Identify the blood parasite species.
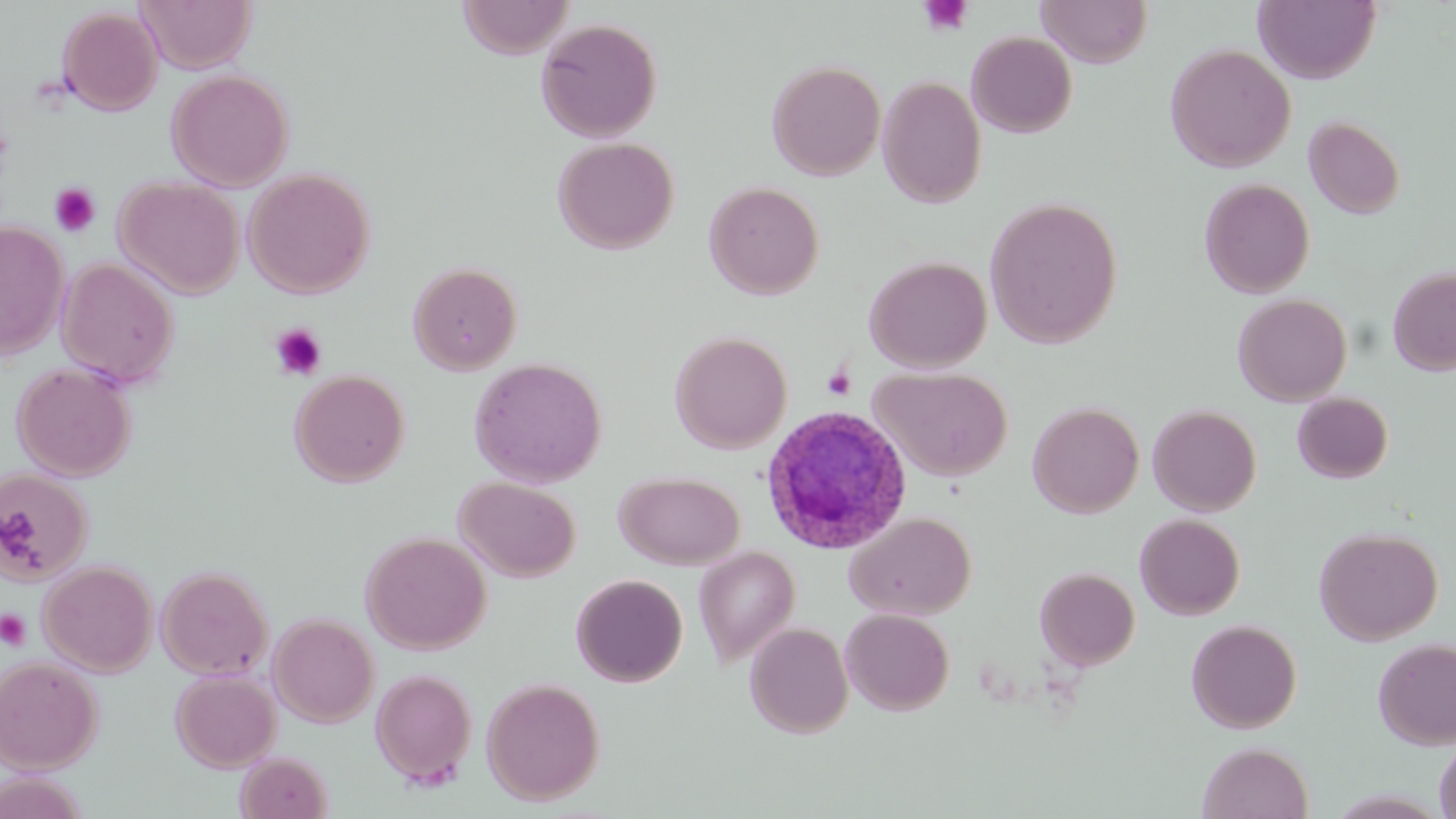
Plasmodium ovale.

preparation: thin blood smear
field_of_view: one of a larger specimen
image_size: 1456×819 pixels
uninfected_red_blood_cell_locations: 'approximate bounding boxes as (x1,y1)-(x2,y2) corner pairs in pixels: (137,0)-(256,73), (456,0)-(574,58), (1037,0)-(1152,68), (1254,0)-(1380,83), (56,6)-(163,116), (535,18)-(663,143), (966,30)-(1077,138), (1165,43)-(1296,173), (766,59)-(886,180), (166,68)-(294,191), (878,75)-(987,208), (1303,116)-(1405,219), (552,137)-(679,255), (243,167)-(375,299), (114,176)-(244,299), (1199,177)-(1315,298), (704,180)-(824,300), (984,196)-(1123,349), (0,220)-(69,360), (864,254)-(992,373), (57,257)-(180,388), (408,261)-(522,375), (1388,266)-(1456,376), (1232,292)-(1352,406), (669,330)-(792,454), (469,356)-(607,487), (12,362)-(136,481), (872,366)-(1012,481), (290,369)-(410,487), (1292,392)-(1393,483), (1027,402)-(1144,518), (1148,404)-(1262,516), (0,469)-(93,584), (615,471)-(745,569), (454,477)-(581,582), (845,511)-(975,621), (1135,513)-(1245,620), (1313,526)-(1443,645), (361,531)-(491,654), (694,546)-(801,668), (39,560)-(158,677), (156,564)-(273,680), (1034,566)-(1140,670), (571,574)-(688,687), (840,608)-(955,715), (268,613)-(379,727), (1186,618)-(1302,733), (744,622)-(854,738), (1372,637)-(1456,750), (0,655)-(103,773), (370,668)-(477,787), (170,669)-(281,772), (481,677)-(605,805), (1434,736)-(1456,819), (1197,741)-(1314,819), (236,751)-(333,818)'
stain: May-Grünwald-Giemsa
modality: light microscopy
magnification: 1000x
plasmodium_ovale_infected_red_blood_cell_locations: 'approximate bounding boxes as (x1,y1)-(x2,y2) corner pairs in pixels: (760,403)-(913,554)'
platelet_locations: 'approximate bounding boxes as (x1,y1)-(x2,y2) corner pairs in pixels: (918,0)-(974,37), (49,182)-(102,238), (269,323)-(328,381), (822,367)-(856,401), (0,609)-(32,651)'